Locate every Plasmodium falciparum-infected red blood cell.
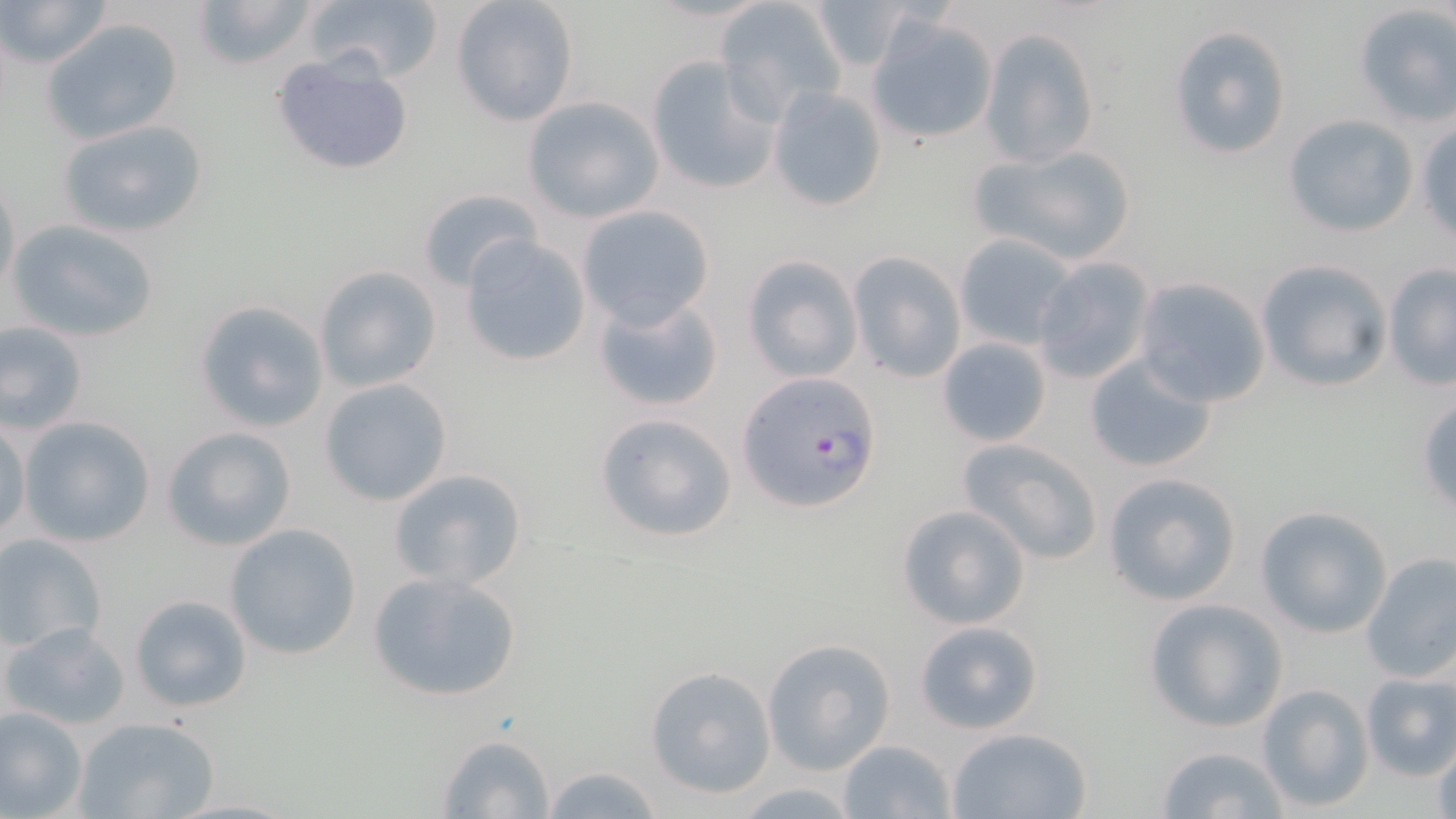
Approximate bounding boxes as (x1,y1)-(x2,y2) corner pairs in pixels.
Plasmodium falciparum-infected red blood cells: (736,372)-(882,513).

Summary:
  - Uninfected red blood cell locations: (3,0)-(115,70), (189,0)-(324,72), (302,0)-(443,84), (450,0)-(579,127), (809,0)-(916,73), (716,1)-(848,121), (1351,4)-(1456,126), (866,13)-(999,146), (40,17)-(185,146), (1166,24)-(1292,160), (980,29)-(1101,168), (270,51)-(415,177), (645,55)-(779,195), (766,84)-(889,212), (521,95)-(664,223), (1283,114)-(1417,237), (1414,116)-(1456,239), (57,118)-(207,241), (968,141)-(1138,268), (1,179)-(20,306), (416,187)-(545,292), (577,204)-(714,329), (6,217)-(160,343), (459,233)-(591,368), (953,233)-(1078,350), (847,252)-(967,384), (742,255)-(864,381), (1029,257)-(1156,386), (1254,259)-(1392,392), (1383,264)-(1456,390), (314,265)-(442,394), (1133,276)-(1272,409), (590,292)-(725,415), (193,301)-(329,433), (0,320)-(89,435), (937,336)-(1053,445), (1084,352)-(1219,473), (319,378)-(454,506), (1415,397)-(1456,515), (591,411)-(739,545), (1,415)-(30,542), (18,416)-(156,547), (162,426)-(297,551), (956,435)-(1104,565), (389,468)-(528,591), (1101,470)-(1243,607), (895,504)-(1031,631), (1253,505)-(1390,638), (225,524)-(361,660), (0,533)-(108,655), (1359,552)-(1456,684), (366,570)-(525,704), (128,593)-(253,714), (1143,598)-(1289,733), (912,620)-(1044,735), (5,622)-(129,729), (762,637)-(895,776), (645,666)-(777,797), (1357,670)-(1456,779), (1255,683)-(1375,812), (0,705)-(88,817), (74,716)-(221,819), (946,727)-(1096,818), (435,732)-(556,818), (1429,732)-(1456,819), (838,738)-(956,818), (1154,744)-(1291,817), (538,763)-(664,819)
  - Slide-level diagnosis: Plasmodium falciparum
  - Image size: 1456×819 pixels
  - Stain: May-Grünwald-Giemsa
  - Magnification: 1000x
  - Modality: light microscopy
  - Preparation: thin blood film
  - Field of view: one of a larger specimen